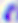

Summary:
  - Identification: Toxoplasma gondii
  - Modality: photomicrograph
  - Magnification: 400x